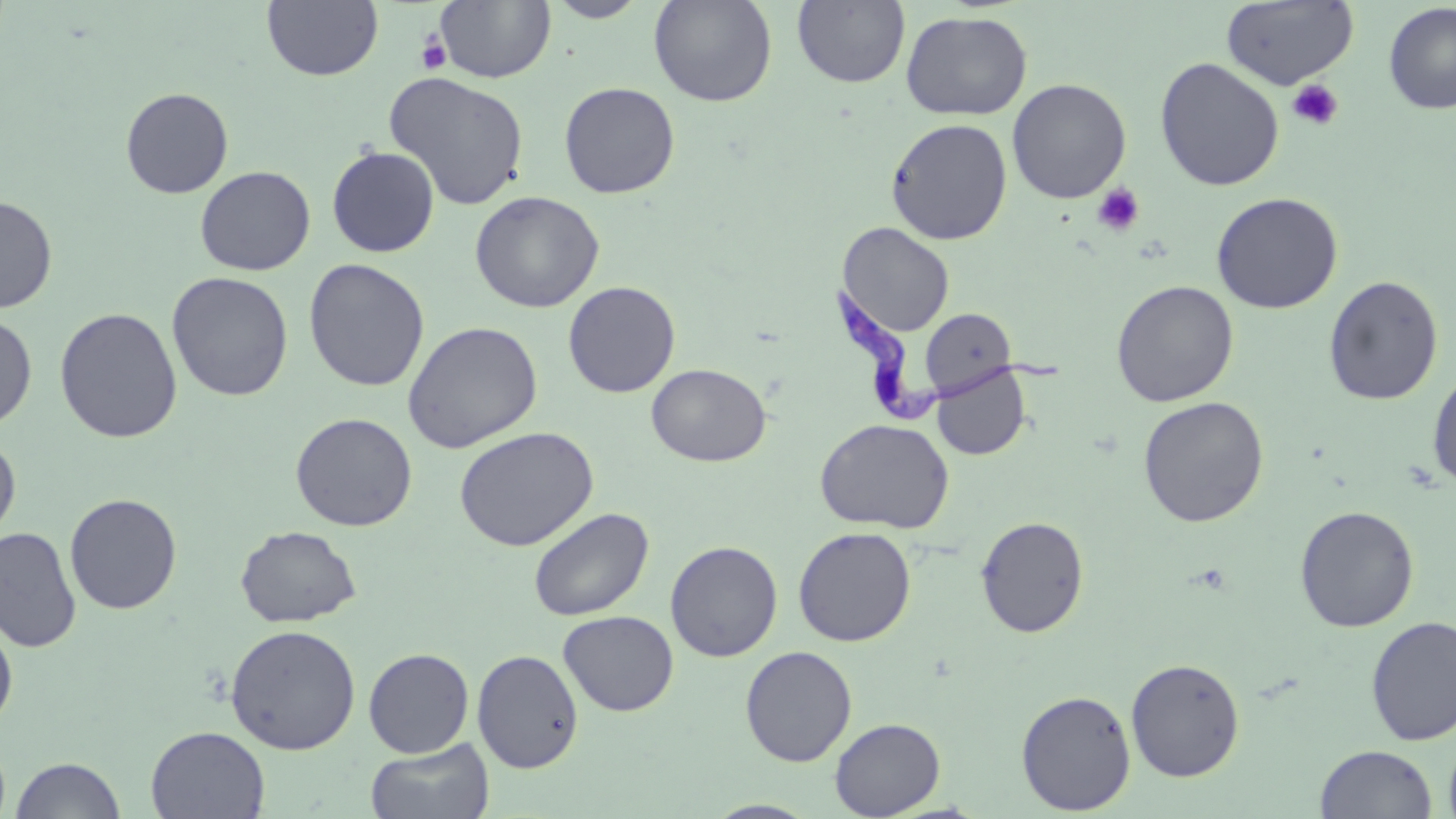

Approximate bounding boxes as (x1,y1)-(x2,y2) corner pairs in pixels. Trypanosoma brucei locations: (831,282)-(1066,426). Uninfected red blood cell locations: (544,0)-(652,22), (648,0)-(778,107), (792,0)-(910,88), (1220,0)-(1359,91), (262,1)-(383,81), (436,1)-(556,84), (1382,3)-(1456,115), (901,11)-(1033,121), (1154,57)-(1284,192), (383,71)-(529,211), (1007,78)-(1131,204), (559,81)-(680,199), (120,87)-(234,198), (886,117)-(1013,245), (326,145)-(440,257), (194,165)-(315,276), (470,191)-(604,313), (1210,191)-(1344,314), (0,194)-(58,313), (837,222)-(954,337), (303,258)-(430,392), (166,271)-(294,402), (1323,275)-(1443,406), (1111,280)-(1239,406), (563,281)-(681,398), (54,307)-(183,443), (920,308)-(1016,398), (0,312)-(37,430), (402,320)-(543,453), (646,363)-(771,467), (931,365)-(1030,460), (1427,367)-(1456,491), (1138,396)-(1269,527), (290,412)-(417,531), (815,418)-(954,534), (453,426)-(599,551), (0,433)-(21,546), (64,493)-(182,614), (1294,505)-(1419,632), (527,507)-(654,621), (976,515)-(1090,638), (235,525)-(362,627), (0,526)-(81,653), (793,526)-(916,647), (665,540)-(782,662), (558,609)-(680,715), (1365,615)-(1456,746), (0,617)-(18,732), (225,624)-(361,755), (739,645)-(857,766), (363,647)-(474,757), (472,649)-(583,773), (1126,658)-(1245,781), (1016,689)-(1136,814), (830,717)-(945,818), (145,726)-(270,818), (1444,733)-(1456,819), (364,737)-(495,819), (1315,744)-(1437,819), (10,756)-(126,819), (702,799)-(821,818). Platelet locations: (416,33)-(452,75), (1287,79)-(1344,130), (1091,182)-(1146,236). Slide-level diagnosis: Trypanosoma brucei. Optical microscopy. Thin blood smear. May-Grünwald-Giemsa-stained preparation. Image is 1456×819 pixels. One field of a larger specimen. 1000x magnification.